Locate every blood parasite and identify its species.
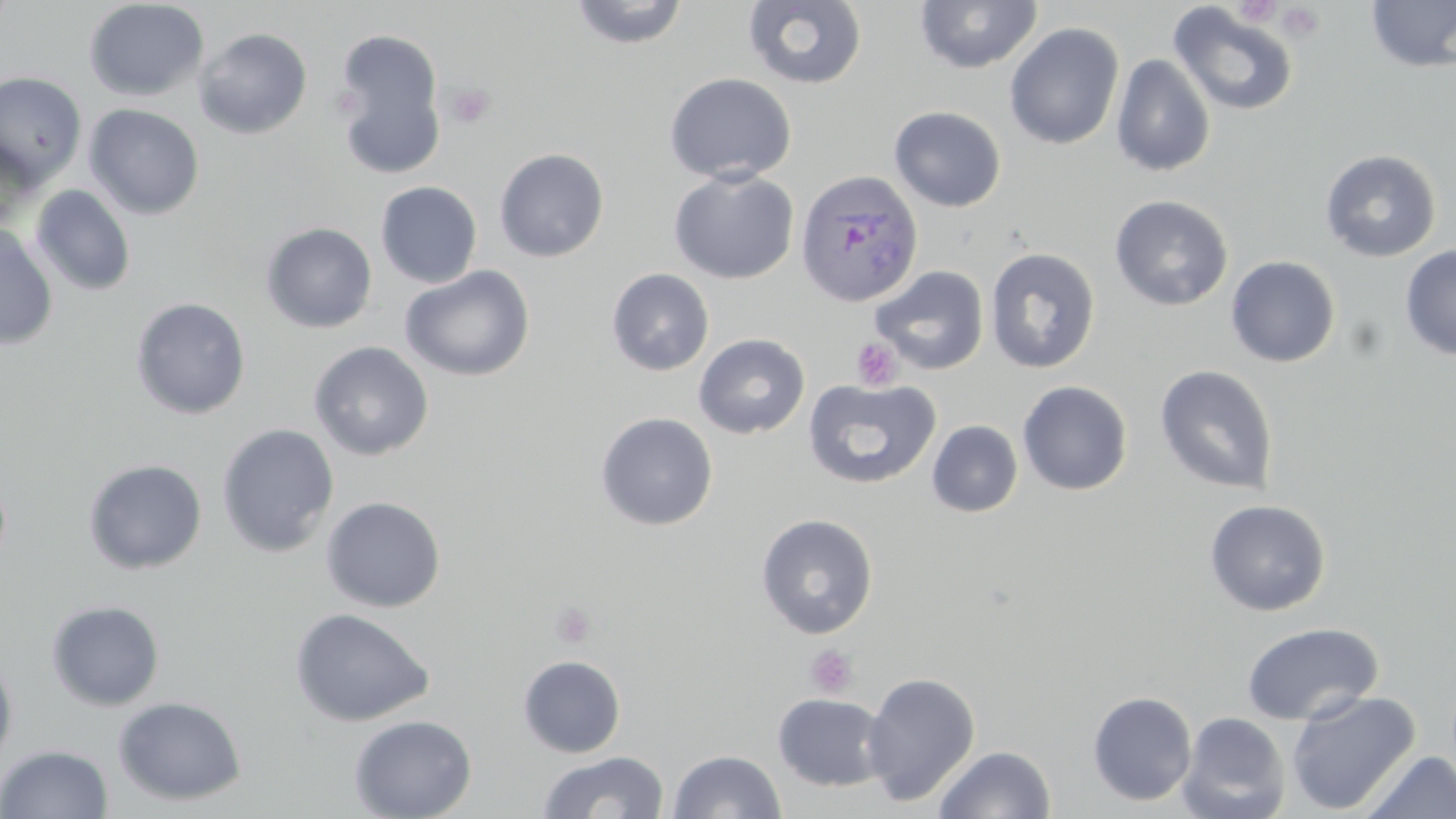

Approximate bounding boxes as named x1/y1/x2/y2 corners in pixels.
Plasmodium ovale-infected red blood cells: (x1=795, y1=169, x2=924, y2=308).
No Plasmodium falciparum, Plasmodium malariae, Plasmodium vivax, Babesia divergens, or Trypanosoma brucei observed.

Platelet locations: (x1=1276, y1=3, x2=1326, y2=42), (x1=447, y1=82, x2=495, y2=130), (x1=851, y1=338, x2=902, y2=390), (x1=549, y1=602, x2=597, y2=648), (x1=804, y1=644, x2=858, y2=699). Uninfected red blood cell locations: (x1=83, y1=0, x2=209, y2=102), (x1=567, y1=0, x2=691, y2=49), (x1=914, y1=0, x2=1044, y2=75), (x1=1364, y1=0, x2=1456, y2=74), (x1=743, y1=1, x2=867, y2=90), (x1=1168, y1=3, x2=1300, y2=118), (x1=1004, y1=23, x2=1124, y2=150), (x1=194, y1=28, x2=312, y2=140), (x1=332, y1=28, x2=448, y2=179), (x1=1110, y1=53, x2=1216, y2=177), (x1=0, y1=71, x2=87, y2=188), (x1=663, y1=72, x2=796, y2=184), (x1=84, y1=103, x2=205, y2=220), (x1=889, y1=105, x2=1006, y2=212), (x1=0, y1=139, x2=40, y2=235), (x1=494, y1=148, x2=609, y2=262), (x1=1320, y1=149, x2=1442, y2=262), (x1=668, y1=168, x2=799, y2=284), (x1=375, y1=181, x2=482, y2=288), (x1=30, y1=185, x2=136, y2=296), (x1=1109, y1=194, x2=1234, y2=311), (x1=260, y1=222, x2=377, y2=334), (x1=0, y1=224, x2=58, y2=350), (x1=1400, y1=244, x2=1456, y2=360), (x1=985, y1=247, x2=1100, y2=373), (x1=1225, y1=255, x2=1341, y2=368), (x1=400, y1=265, x2=536, y2=382), (x1=870, y1=265, x2=989, y2=374), (x1=606, y1=268, x2=714, y2=376), (x1=130, y1=297, x2=251, y2=420), (x1=693, y1=333, x2=810, y2=439), (x1=308, y1=341, x2=434, y2=461), (x1=1155, y1=365, x2=1279, y2=495), (x1=803, y1=377, x2=942, y2=490), (x1=1017, y1=380, x2=1133, y2=496), (x1=595, y1=412, x2=718, y2=531), (x1=927, y1=420, x2=1023, y2=517), (x1=217, y1=423, x2=339, y2=557), (x1=83, y1=458, x2=207, y2=575), (x1=320, y1=496, x2=446, y2=613), (x1=1204, y1=498, x2=1331, y2=616), (x1=756, y1=513, x2=878, y2=639), (x1=46, y1=600, x2=165, y2=711), (x1=291, y1=607, x2=434, y2=727), (x1=1241, y1=622, x2=1384, y2=726), (x1=0, y1=652, x2=18, y2=775), (x1=518, y1=654, x2=625, y2=758), (x1=861, y1=671, x2=981, y2=806), (x1=1286, y1=690, x2=1421, y2=815), (x1=1087, y1=691, x2=1197, y2=806), (x1=772, y1=693, x2=890, y2=792), (x1=113, y1=696, x2=247, y2=806), (x1=1177, y1=711, x2=1291, y2=819), (x1=349, y1=714, x2=477, y2=819), (x1=0, y1=744, x2=113, y2=819), (x1=933, y1=745, x2=1056, y2=819), (x1=668, y1=749, x2=786, y2=818), (x1=537, y1=750, x2=669, y2=818), (x1=1361, y1=750, x2=1456, y2=818). Slide-level diagnosis: Plasmodium ovale. 1000x magnification. May-Grünwald-Giemsa stain. Single field of view. Thin blood film. Light microscopy. Image is 1456×819 pixels.